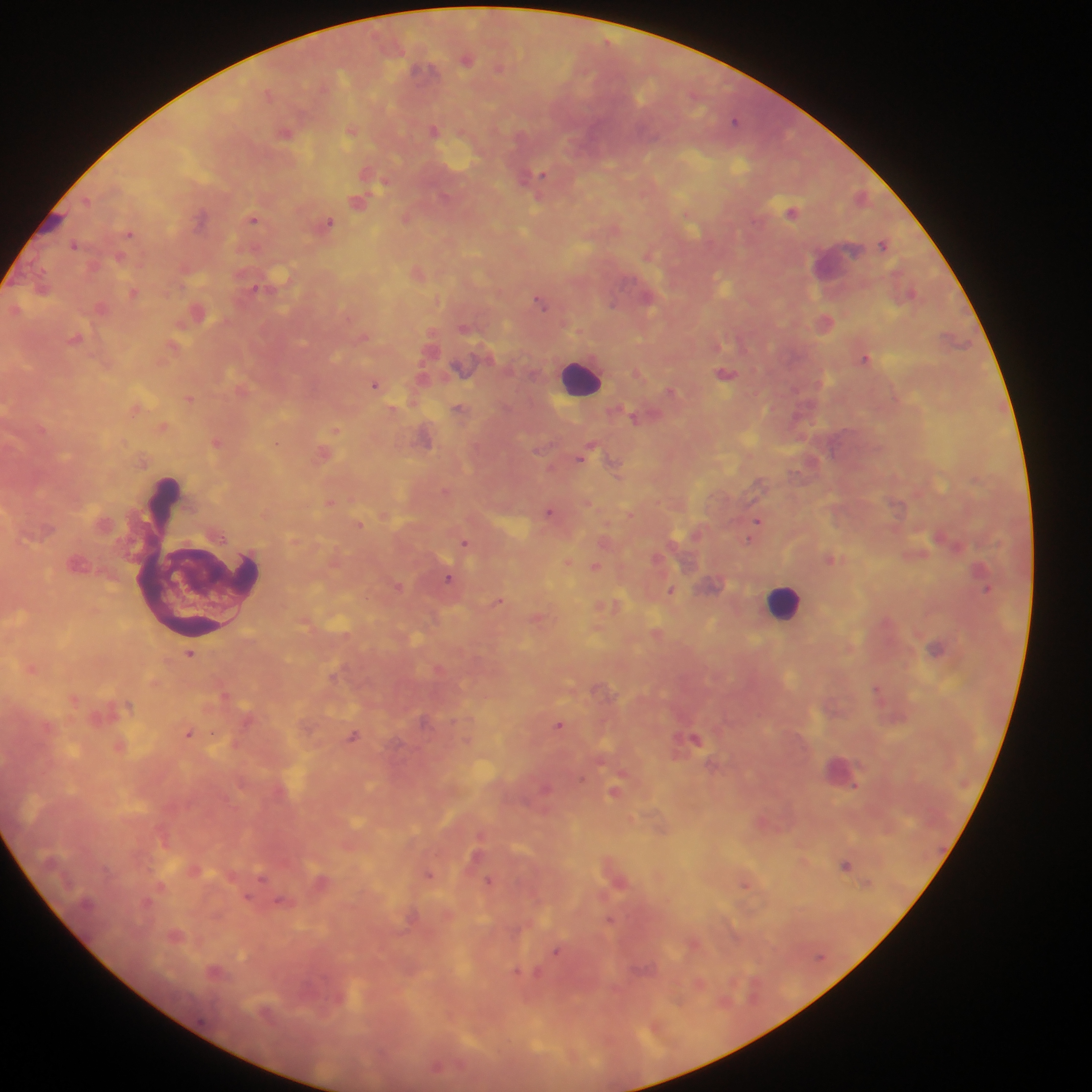

Approximate centers as (x, y) in pixels. Leukocyte locations: (582, 378), (783, 602), (840, 770). Plasmodium parasite locations: (466, 58), (500, 68), (268, 93), (735, 121), (352, 129), (434, 130), (286, 132), (370, 173), (533, 181), (862, 196), (359, 200), (792, 212), (407, 217), (200, 218), (254, 218), (328, 223), (129, 233), (884, 244), (75, 245), (649, 253), (418, 272), (42, 288), (255, 288), (134, 293), (912, 293), (541, 299), (101, 307), (196, 312), (825, 322), (466, 328), (77, 338), (173, 346), (866, 357), (638, 372), (726, 373), (375, 384), (672, 391), (189, 398), (136, 407), (460, 409), (393, 410), (635, 417), (162, 426), (336, 430), (425, 436), (217, 442), (277, 442), (324, 453), (585, 454), (616, 467), (446, 491), (331, 501), (550, 511), (385, 515), (758, 520), (359, 524), (749, 539), (606, 540), (466, 542), (830, 558), (568, 562), (596, 565), (450, 578), (398, 585), (987, 590), (671, 591), (499, 601), (609, 606), (539, 618), (657, 633), (937, 648), (190, 654), (32, 667), (333, 676), (879, 689), (226, 693), (74, 699), (559, 725), (189, 732), (353, 736), (696, 738), (119, 746), (545, 787), (615, 791), (846, 865), (195, 869), (429, 874), (489, 880), (618, 881), (320, 882), (746, 883), (249, 898), (283, 901), (611, 920), (176, 936), (694, 943), (557, 951), (215, 971), (536, 973), (699, 982), (438, 1066). Mobile-phone photograph taken through the microscope. Thick blood smear. Image is 1092×1092 pixels. Sample from Ghana. One field of view.